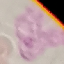
Malaria status: uninfected. Automatically extracted cell patch, resized to 64 × 64 pixels. Acquired by smartphone through the microscope eyepiece. Thin blood film. Giemsa-stained preparation.